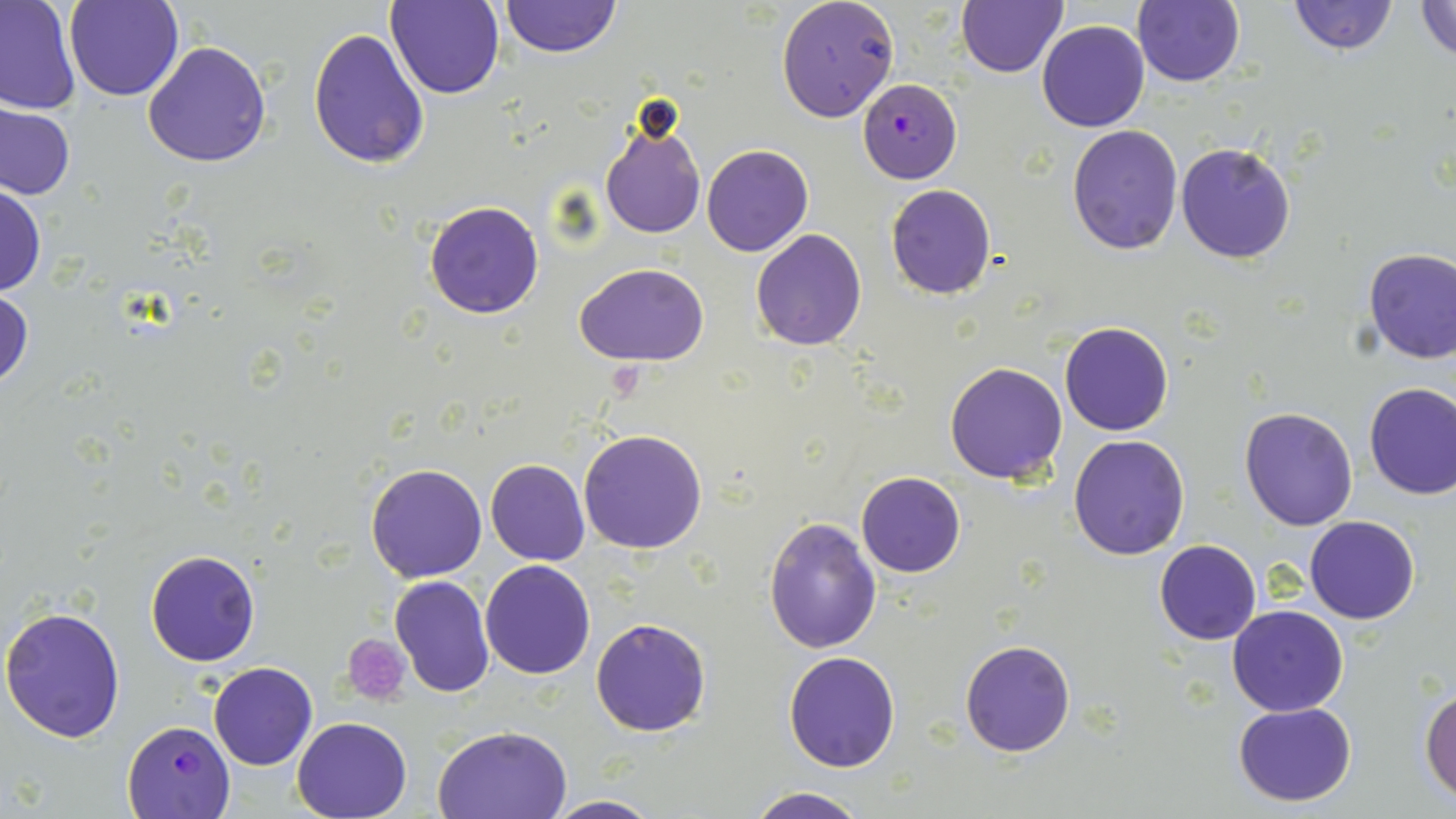
Summary:
  - Coordinate format: approximate bounding boxes as [x1, y1, x2, y2] in pixels
  - Plasmodium falciparum-infected red blood cell locations: [857, 79, 962, 183], [122, 720, 237, 819]
  - Uninfected red blood cell locations: [63, 0, 182, 101], [499, 0, 620, 58], [776, 0, 899, 122], [956, 0, 1068, 78], [1134, 0, 1244, 86], [1288, 0, 1398, 54], [1413, 0, 1456, 61], [385, 1, 506, 100], [0, 2, 80, 115], [1037, 21, 1150, 132], [307, 27, 429, 170], [143, 41, 273, 168], [0, 103, 75, 201], [598, 122, 705, 239], [1067, 123, 1182, 254], [1176, 142, 1296, 264], [701, 143, 814, 257], [0, 182, 45, 297], [885, 184, 997, 300], [423, 200, 545, 319], [750, 229, 867, 350], [1361, 248, 1456, 365], [576, 263, 710, 365], [0, 285, 33, 396], [1060, 322, 1173, 436], [944, 361, 1068, 483], [1363, 382, 1456, 500], [1239, 407, 1359, 529], [578, 428, 708, 554], [1068, 434, 1190, 560], [485, 458, 590, 565], [367, 464, 487, 583], [856, 472, 966, 576], [764, 515, 883, 655], [1304, 516, 1420, 624], [1155, 539, 1261, 645], [145, 549, 261, 667], [480, 559, 596, 679], [390, 575, 495, 697], [0, 604, 127, 744], [1227, 604, 1348, 716], [590, 617, 711, 737], [959, 640, 1075, 757], [783, 649, 900, 771], [209, 661, 317, 770], [1420, 686, 1455, 802], [1232, 700, 1357, 805], [291, 716, 413, 819], [433, 724, 572, 817], [743, 788, 873, 819], [543, 796, 665, 818]
  - Platelet locations: [340, 635, 413, 704]
  - Slide-level diagnosis: Plasmodium falciparum
  - Stain: May-Grünwald-Giemsa
  - Magnification: 1000x
  - Preparation: thin blood film
  - Modality: light microscopy
  - Image size: 1456×819 pixels
  - Field of view: single